Classify this cell by malaria status.
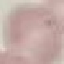

It is uninfected.

Acquired by smartphone through the microscope eyepiece. Giemsa stain. Cell patch, automatically extracted from a larger field of view and resized to 64 × 64 pixels. Thin blood film.